Classify this cell by malaria status.
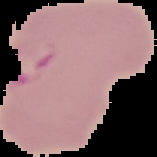
It is parasitized.

Image is 157×157 pixels. From a thin blood smear. Segmented cell region on a black background.